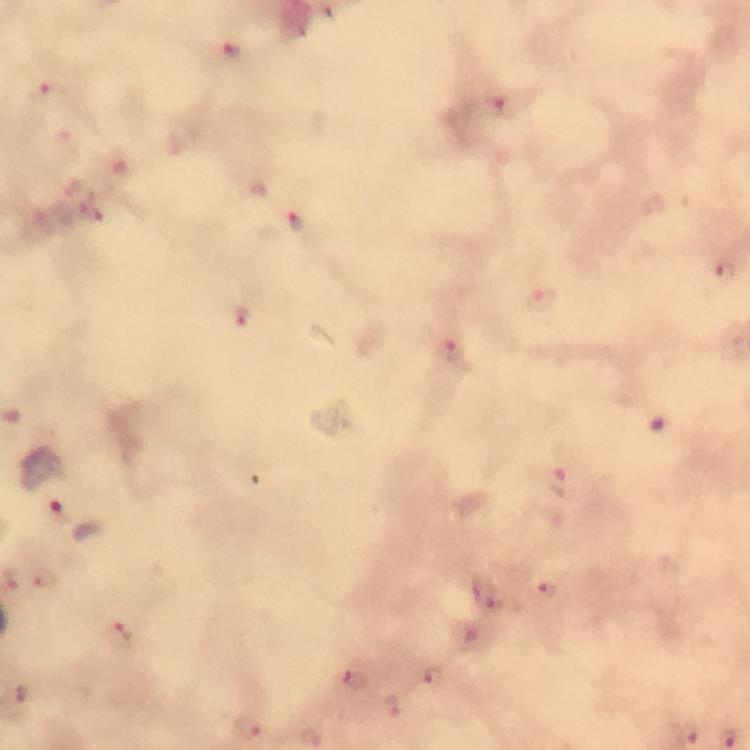

malaria_parasite_locations: 'approximate object centers, in pixels from the top-left corner: (x=230, y=50), (x=47, y=93), (x=497, y=105), (x=293, y=222), (x=724, y=266), (x=541, y=301), (x=242, y=316), (x=451, y=350), (x=559, y=483), (x=61, y=512), (x=43, y=576), (x=550, y=591), (x=117, y=637), (x=432, y=678), (x=355, y=680), (x=246, y=726), (x=686, y=733), (x=312, y=738)'
context: from a malaria diagnostic workup
immersion_oil: applied
stain: Giemsa
preparation: thick blood film
capture: smartphone mounted on the microscope
magnification: 100x
cropped_from: one field of view
image_size: 750×750 pixels